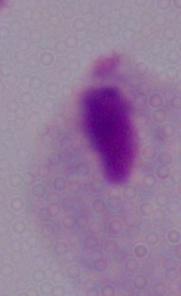
Captured at 1000x magnification. Photomicrograph. A trichomonad is shown.